Outline each blood parasite and name the species.
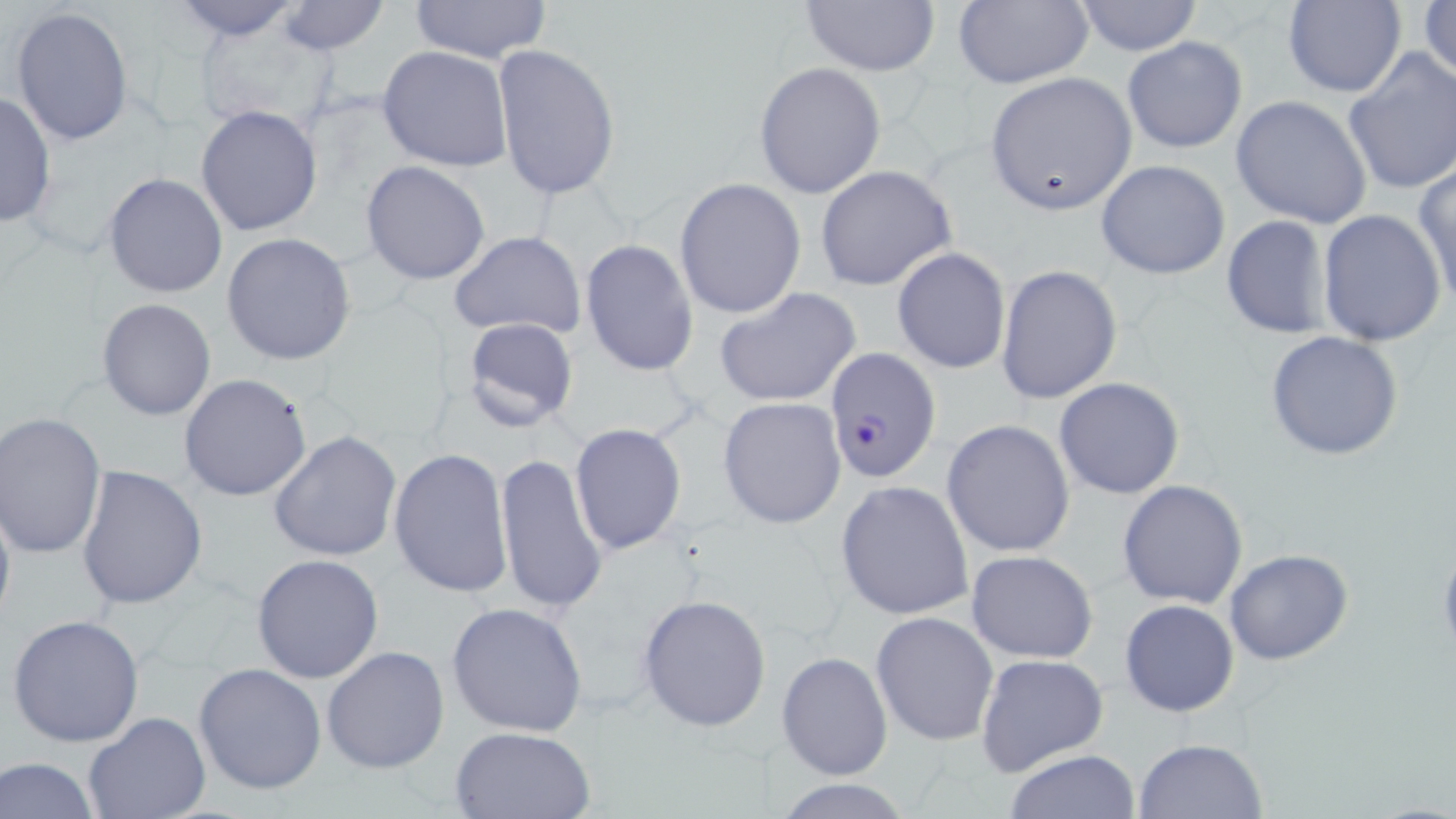
Approximate bounding boxes as named x1/y1/x2/y2 corners in pixels.
Plasmodium falciparum-infected red blood cells: (x1=825, y1=347, x2=941, y2=482).
No Plasmodium ovale, Plasmodium malariae, Plasmodium vivax, Babesia divergens, or Trypanosoma brucei observed.

Uninfected red blood cell locations: (x1=168, y1=0, x2=307, y2=42), (x1=277, y1=0, x2=389, y2=55), (x1=410, y1=0, x2=553, y2=65), (x1=796, y1=0, x2=941, y2=75), (x1=952, y1=0, x2=1095, y2=90), (x1=1070, y1=0, x2=1205, y2=55), (x1=1418, y1=0, x2=1455, y2=91), (x1=1282, y1=1, x2=1404, y2=97), (x1=11, y1=6, x2=134, y2=147), (x1=193, y1=16, x2=337, y2=132), (x1=1122, y1=35, x2=1248, y2=155), (x1=492, y1=44, x2=621, y2=201), (x1=377, y1=46, x2=513, y2=172), (x1=1344, y1=49, x2=1456, y2=196), (x1=754, y1=61, x2=887, y2=198), (x1=988, y1=72, x2=1137, y2=208), (x1=0, y1=91, x2=56, y2=229), (x1=1231, y1=95, x2=1372, y2=230), (x1=196, y1=104, x2=323, y2=236), (x1=1096, y1=159, x2=1232, y2=279), (x1=360, y1=161, x2=490, y2=285), (x1=1413, y1=163, x2=1456, y2=311), (x1=814, y1=165, x2=956, y2=291), (x1=103, y1=171, x2=230, y2=300), (x1=675, y1=177, x2=805, y2=321), (x1=1317, y1=208, x2=1447, y2=346), (x1=1220, y1=213, x2=1334, y2=341), (x1=449, y1=231, x2=588, y2=340), (x1=221, y1=232, x2=357, y2=365), (x1=580, y1=239, x2=700, y2=377), (x1=891, y1=247, x2=1011, y2=376), (x1=996, y1=264, x2=1121, y2=403), (x1=715, y1=286, x2=863, y2=407), (x1=96, y1=299, x2=216, y2=420), (x1=459, y1=316, x2=579, y2=432), (x1=1263, y1=331, x2=1404, y2=462), (x1=179, y1=373, x2=312, y2=502), (x1=1053, y1=377, x2=1185, y2=500), (x1=719, y1=397, x2=847, y2=528), (x1=1, y1=413, x2=106, y2=558), (x1=941, y1=419, x2=1076, y2=559), (x1=570, y1=422, x2=687, y2=555), (x1=268, y1=431, x2=402, y2=560), (x1=388, y1=448, x2=512, y2=598), (x1=493, y1=451, x2=608, y2=617), (x1=76, y1=464, x2=208, y2=610), (x1=834, y1=479, x2=975, y2=621), (x1=1118, y1=479, x2=1249, y2=609), (x1=0, y1=487, x2=16, y2=639), (x1=1224, y1=548, x2=1354, y2=666), (x1=965, y1=551, x2=1098, y2=662), (x1=251, y1=554, x2=385, y2=683), (x1=637, y1=593, x2=772, y2=732), (x1=1119, y1=599, x2=1239, y2=717), (x1=445, y1=602, x2=588, y2=738), (x1=871, y1=611, x2=999, y2=746), (x1=6, y1=614, x2=145, y2=747), (x1=322, y1=646, x2=451, y2=774), (x1=777, y1=650, x2=893, y2=781), (x1=975, y1=653, x2=1109, y2=776), (x1=194, y1=663, x2=327, y2=796), (x1=82, y1=712, x2=210, y2=819), (x1=449, y1=727, x2=595, y2=818), (x1=1132, y1=737, x2=1269, y2=819), (x1=1002, y1=749, x2=1141, y2=818), (x1=1, y1=756, x2=101, y2=819), (x1=766, y1=778, x2=924, y2=817). Slide-level diagnosis: Plasmodium falciparum. Image is 1456×819 pixels. May-Grünwald-Giemsa-stained preparation. Light microscopy. One field of a larger specimen. 1000x magnification. Thin blood film.